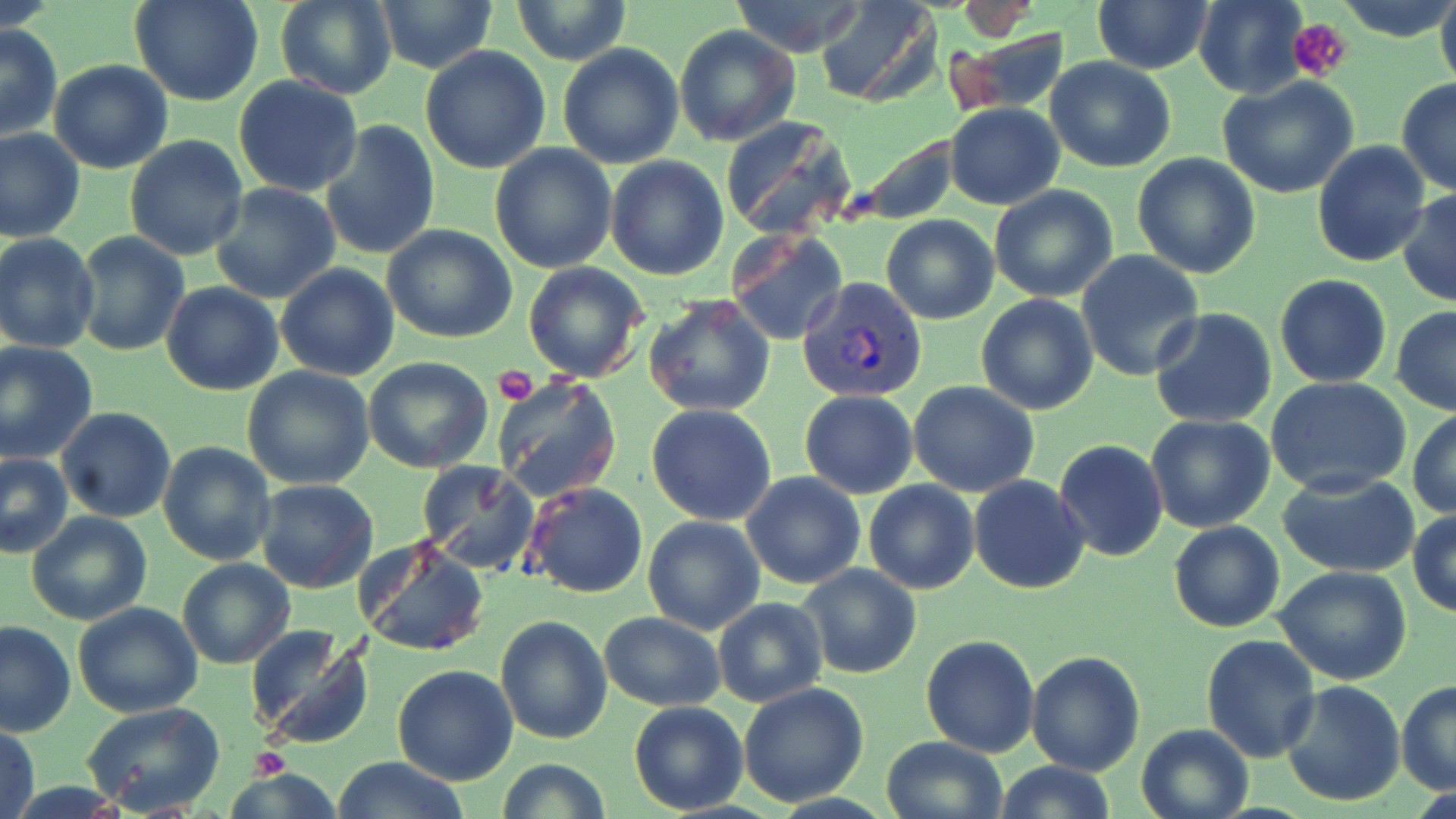
Summary:
  - Coordinate format: approximate bounding boxes as (x1, y1, x2, y2) in pixels
  - Plasmodium vivax-infected red blood cell locations: (797, 277, 930, 403)
  - Platelet locations: (1289, 19, 1352, 82), (493, 365, 537, 406), (250, 748, 288, 778)
  - Uninfected red blood cell locations: (131, 0, 263, 107), (276, 0, 396, 100), (372, 0, 501, 73), (729, 0, 867, 56), (818, 0, 941, 107), (1195, 0, 1307, 99), (1336, 0, 1452, 41), (1435, 0, 1456, 97), (513, 1, 629, 65), (1092, 2, 1213, 75), (0, 23, 62, 140), (674, 26, 801, 148), (950, 30, 1071, 116), (558, 43, 685, 169), (419, 46, 551, 174), (1044, 55, 1176, 173), (48, 58, 174, 175), (233, 76, 363, 196), (1217, 76, 1361, 198), (1395, 79, 1456, 196), (945, 103, 1064, 209), (723, 118, 858, 242), (318, 121, 441, 261), (0, 127, 84, 243), (843, 130, 960, 225), (124, 136, 250, 260), (1312, 141, 1430, 266), (490, 144, 617, 273), (1132, 153, 1261, 279), (604, 155, 728, 280), (210, 182, 341, 304), (989, 184, 1119, 302), (1396, 191, 1456, 307), (881, 214, 999, 324), (382, 224, 518, 345), (726, 228, 848, 346), (73, 230, 191, 355), (0, 233, 100, 354), (1078, 251, 1205, 381), (523, 263, 647, 383), (276, 264, 400, 382), (1274, 274, 1393, 387), (160, 281, 285, 396), (976, 293, 1099, 416), (644, 295, 776, 419), (1392, 306, 1456, 415), (1149, 308, 1277, 428), (0, 341, 98, 464), (363, 358, 493, 474), (241, 366, 375, 490), (495, 378, 621, 501), (1266, 378, 1411, 497), (908, 379, 1041, 497), (798, 390, 919, 500), (646, 403, 777, 526), (57, 408, 176, 524), (1408, 408, 1456, 520), (1144, 413, 1276, 533), (1054, 439, 1169, 563), (157, 440, 276, 566), (0, 453, 73, 557), (417, 461, 540, 577), (742, 473, 866, 590), (1279, 473, 1420, 577), (969, 475, 1089, 593), (255, 480, 378, 594), (863, 480, 979, 595), (525, 481, 648, 599), (1408, 510, 1455, 617), (27, 511, 152, 626), (642, 516, 766, 636), (1169, 521, 1285, 632), (355, 535, 490, 657), (177, 558, 296, 669), (796, 563, 924, 680), (1272, 565, 1413, 685), (713, 597, 828, 708), (73, 601, 202, 717), (600, 612, 726, 710), (496, 615, 612, 742), (0, 620, 75, 737), (246, 625, 376, 750), (1201, 634, 1321, 763), (919, 635, 1039, 757), (1026, 650, 1145, 775), (394, 665, 519, 784), (1279, 680, 1406, 807), (1396, 680, 1456, 795), (738, 683, 870, 807), (628, 702, 750, 815), (83, 703, 228, 816), (1135, 722, 1254, 819), (1, 724, 40, 819), (881, 736, 1008, 819), (332, 757, 468, 819), (495, 757, 612, 818), (994, 762, 1119, 819), (222, 766, 339, 817)
  - Slide-level diagnosis: Plasmodium vivax
  - Image size: 1456×819 pixels
  - Field of view: single
  - Preparation: thin blood smear
  - Magnification: 1000x
  - Modality: optical microscopy
  - Stain: May-Grünwald-Giemsa